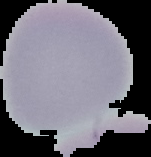

Summary:
  - Image size: 151×157 pixels
  - Preparation: thin blood film
  - Image type: segmented cell region with the area outside set to black
  - Result: no malaria parasites seen